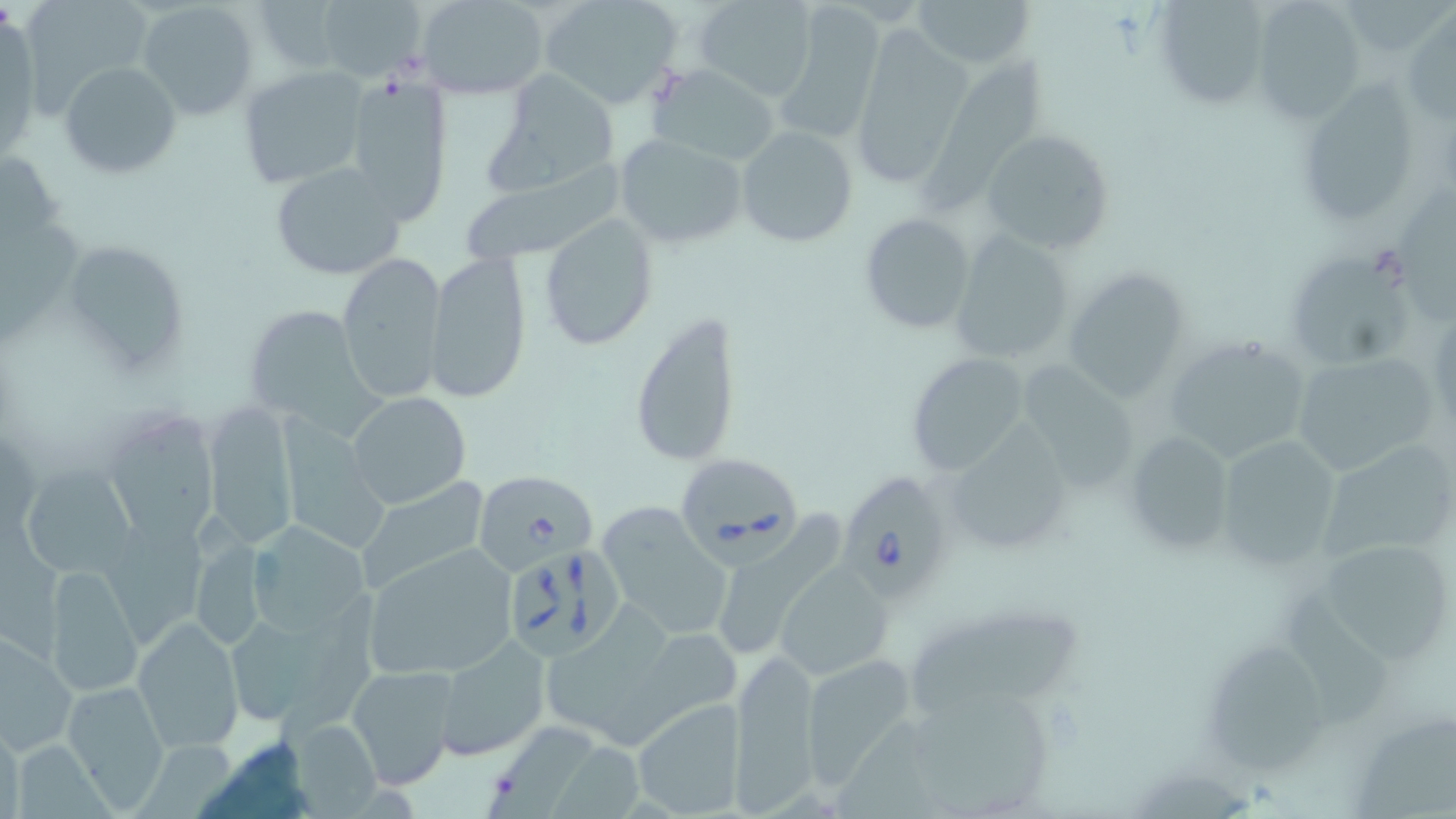

slide-level diagnosis = Babesia divergens
image size = 1456×819 pixels
uninfected red blood cell locations = approximate bounding boxes as named x1/y1/x2/y2 corners in pixels: (x1=24, y1=0, x2=155, y2=105), (x1=538, y1=0, x2=686, y2=109), (x1=694, y1=0, x2=813, y2=101), (x1=911, y1=0, x2=1037, y2=70), (x1=138, y1=1, x2=261, y2=119), (x1=252, y1=1, x2=345, y2=75), (x1=316, y1=1, x2=430, y2=81), (x1=418, y1=1, x2=551, y2=98), (x1=1249, y1=1, x2=1363, y2=122), (x1=1153, y1=2, x2=1272, y2=111), (x1=776, y1=6, x2=887, y2=141), (x1=1404, y1=13, x2=1455, y2=127), (x1=846, y1=27, x2=975, y2=188), (x1=59, y1=61, x2=182, y2=180), (x1=921, y1=62, x2=1046, y2=216), (x1=653, y1=65, x2=780, y2=167), (x1=237, y1=66, x2=368, y2=192), (x1=483, y1=67, x2=624, y2=193), (x1=341, y1=70, x2=456, y2=227), (x1=1309, y1=78, x2=1415, y2=221), (x1=735, y1=125, x2=858, y2=247), (x1=980, y1=128, x2=1115, y2=256), (x1=613, y1=132, x2=747, y2=250), (x1=0, y1=148, x2=67, y2=252), (x1=268, y1=161, x2=408, y2=280), (x1=456, y1=168, x2=623, y2=266), (x1=1402, y1=185, x2=1456, y2=329), (x1=859, y1=212, x2=977, y2=334), (x1=538, y1=214, x2=659, y2=350), (x1=948, y1=231, x2=1078, y2=369), (x1=58, y1=237, x2=193, y2=381), (x1=425, y1=250, x2=532, y2=402), (x1=1283, y1=250, x2=1417, y2=370), (x1=335, y1=251, x2=447, y2=403), (x1=1063, y1=265, x2=1193, y2=402), (x1=238, y1=301, x2=372, y2=426), (x1=628, y1=311, x2=742, y2=470), (x1=1161, y1=335, x2=1315, y2=464), (x1=904, y1=351, x2=1032, y2=478), (x1=1290, y1=351, x2=1444, y2=480), (x1=1022, y1=361, x2=1136, y2=490), (x1=347, y1=392, x2=471, y2=509), (x1=202, y1=399, x2=301, y2=550), (x1=109, y1=415, x2=219, y2=546), (x1=279, y1=418, x2=390, y2=554), (x1=953, y1=423, x2=1068, y2=544), (x1=1120, y1=430, x2=1237, y2=558), (x1=1212, y1=431, x2=1350, y2=575), (x1=1315, y1=440, x2=1455, y2=571), (x1=20, y1=464, x2=139, y2=580), (x1=355, y1=478, x2=491, y2=595), (x1=599, y1=501, x2=732, y2=637), (x1=719, y1=512, x2=846, y2=658), (x1=197, y1=515, x2=266, y2=641), (x1=0, y1=520, x2=74, y2=661), (x1=247, y1=522, x2=373, y2=639), (x1=104, y1=524, x2=205, y2=645), (x1=1317, y1=535, x2=1448, y2=663), (x1=359, y1=543, x2=521, y2=680), (x1=773, y1=563, x2=891, y2=681), (x1=45, y1=564, x2=142, y2=697), (x1=1286, y1=592, x2=1391, y2=730), (x1=275, y1=598, x2=380, y2=741), (x1=543, y1=603, x2=672, y2=745), (x1=911, y1=608, x2=1082, y2=714), (x1=133, y1=616, x2=244, y2=753), (x1=230, y1=623, x2=312, y2=717), (x1=608, y1=628, x2=747, y2=746), (x1=2, y1=630, x2=78, y2=752), (x1=434, y1=636, x2=550, y2=759), (x1=1210, y1=639, x2=1330, y2=776), (x1=729, y1=646, x2=822, y2=811), (x1=798, y1=652, x2=921, y2=788), (x1=346, y1=665, x2=460, y2=791), (x1=62, y1=679, x2=171, y2=810), (x1=908, y1=695, x2=1049, y2=817), (x1=629, y1=697, x2=747, y2=817), (x1=839, y1=713, x2=938, y2=818), (x1=0, y1=718, x2=22, y2=819), (x1=286, y1=719, x2=385, y2=814), (x1=1355, y1=721, x2=1456, y2=819), (x1=489, y1=726, x2=598, y2=819), (x1=13, y1=740, x2=122, y2=819), (x1=135, y1=740, x2=237, y2=819), (x1=549, y1=745, x2=646, y2=819)
magnification = 1000x
Babesia divergens-infected red blood cell locations = approximate bounding boxes as named x1/y1/x2/y2 corners in pixels: (x1=670, y1=458, x2=802, y2=576), (x1=474, y1=469, x2=598, y2=574), (x1=835, y1=471, x2=955, y2=597), (x1=509, y1=551, x2=626, y2=659)
preparation = thin blood film
stain = May-Grünwald-Giemsa
modality = light microscopy
field of view = one of a larger specimen